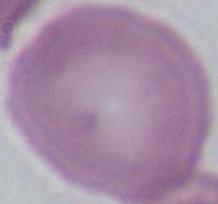
Summary:
  - Magnification: 1000x
  - Modality: micrograph
  - Identification: erythrocyte